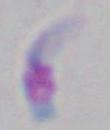
modality: micrograph
identification: Toxoplasma gondii
magnification: 1000x